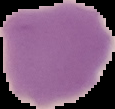

Summary:
  - Malaria status: uninfected
  - Image type: segmented cell region on a black background
  - Preparation: thin blood smear
  - Image size: 115×109 pixels